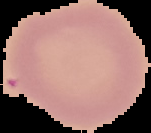

image type = cell region segmented out of the field of view; surrounding area masked to black
preparation = thin blood smear
image size = 151×133 pixels
malaria status = uninfected